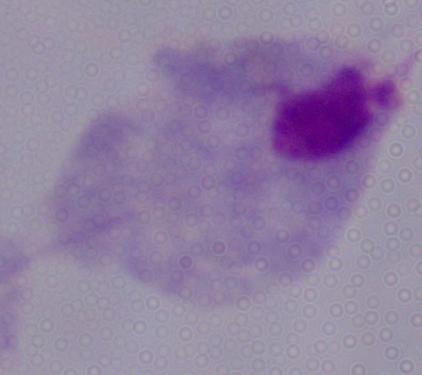
{
  "magnification": "1000x",
  "identification": "trichomonad",
  "modality": "photomicrograph"
}